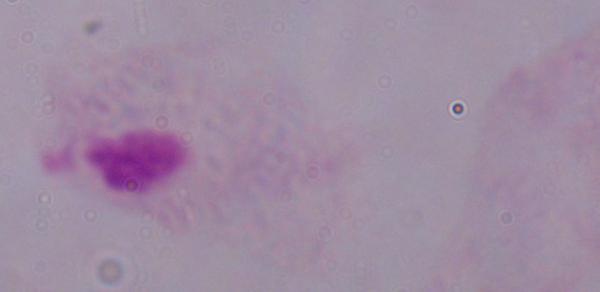
Captured at 1000x magnification. Micrograph. A trichomonad is seen.